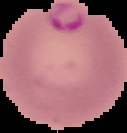
malaria status = parasitized
image type = segmented cell region with the area outside set to black
image size = 127×133 pixels
preparation = thin blood smear